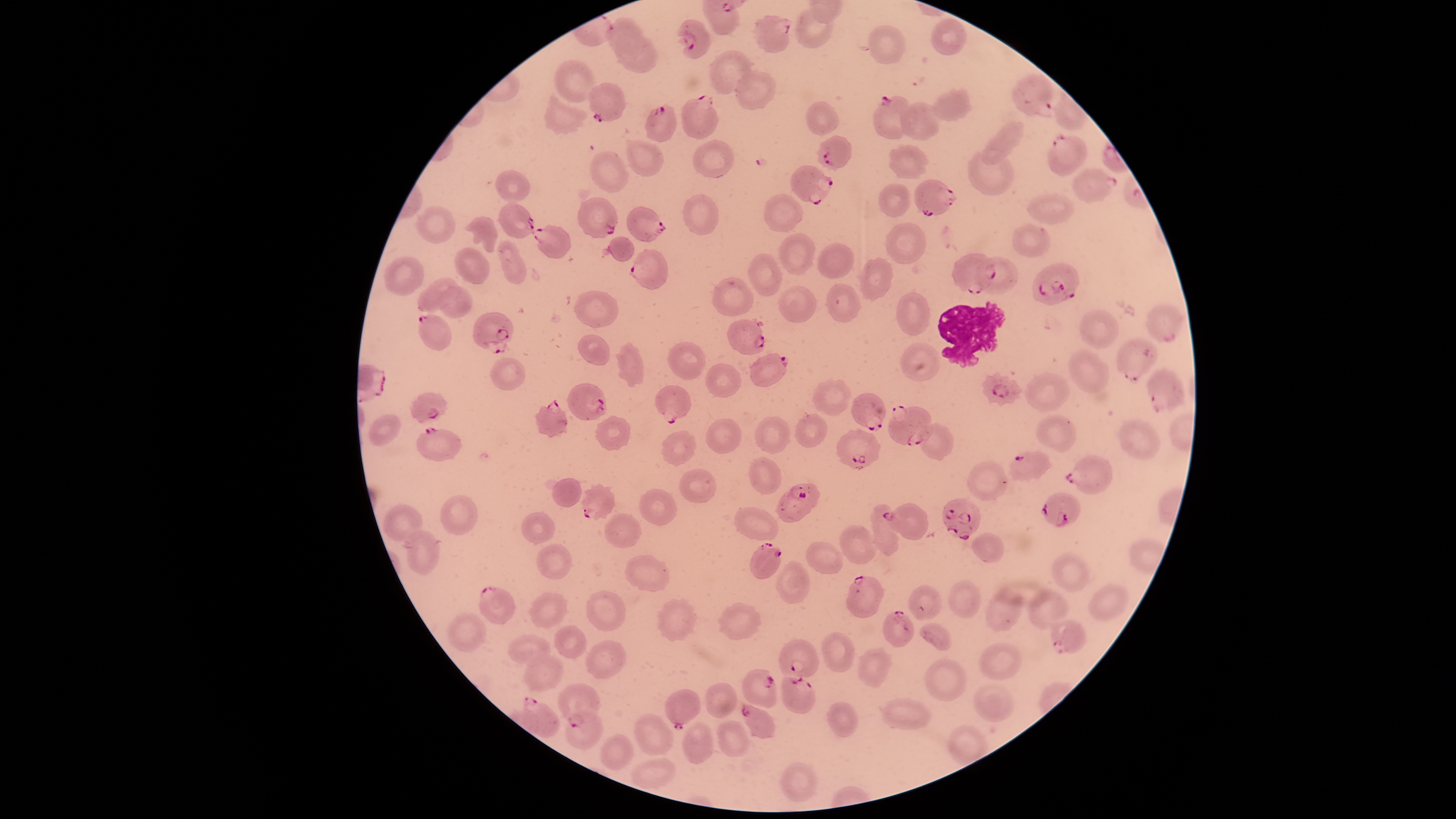

preparation = thin blood film
parasitized red blood cells = approximate bounding boxes as (left, top, right, bottom) in pixels: (753, 15, 792, 53), (677, 19, 710, 58), (1011, 74, 1053, 118), (590, 83, 626, 123), (680, 96, 718, 139), (872, 96, 917, 139), (644, 103, 677, 141), (1048, 132, 1086, 175), (816, 135, 852, 170), (791, 166, 834, 206), (1073, 168, 1118, 203), (915, 180, 955, 216), (579, 197, 617, 238), (498, 202, 534, 238), (626, 206, 666, 242), (532, 224, 570, 258), (629, 248, 666, 290), (952, 254, 995, 295), (1032, 262, 1079, 303), (826, 283, 862, 321), (1148, 303, 1183, 341), (471, 312, 513, 355), (418, 315, 450, 351), (727, 319, 765, 354), (1118, 338, 1158, 382), (748, 354, 789, 387), (1146, 368, 1185, 414), (981, 372, 1021, 407), (568, 383, 606, 420), (655, 385, 694, 424), (411, 392, 447, 422), (850, 392, 886, 431), (534, 400, 568, 437), (888, 405, 932, 445), (416, 427, 463, 460), (836, 429, 880, 470), (1009, 451, 1054, 482), (1065, 455, 1112, 495), (581, 483, 615, 520), (775, 483, 821, 522), (1041, 493, 1080, 526), (942, 498, 980, 540), (881, 502, 929, 539), (750, 541, 781, 579), (845, 575, 884, 619), (479, 586, 515, 624), (882, 610, 914, 647), (1050, 619, 1086, 654), (778, 639, 819, 678), (743, 669, 777, 707), (782, 675, 816, 714), (557, 685, 600, 727), (666, 689, 701, 731), (521, 698, 560, 737), (741, 705, 775, 738)
image size = 1456×819 pixels
uninfected red blood cells = approximate bounding boxes as (left, top, right, bottom) in pixels: (796, 6, 832, 47), (605, 17, 642, 53), (931, 19, 967, 57), (869, 25, 904, 64), (614, 32, 658, 72), (708, 50, 751, 95), (554, 60, 599, 102), (735, 71, 777, 110), (926, 87, 971, 122), (544, 92, 588, 136), (806, 101, 839, 135), (900, 103, 940, 141), (982, 123, 1023, 164), (626, 141, 665, 177), (692, 141, 735, 177), (888, 144, 929, 178), (590, 150, 629, 192), (967, 150, 1014, 194), (495, 170, 530, 202), (879, 184, 910, 218), (1027, 193, 1075, 225), (683, 194, 719, 234), (764, 194, 803, 233), (416, 205, 455, 245), (466, 216, 498, 252), (886, 223, 926, 264), (1013, 224, 1051, 255), (779, 233, 816, 275), (608, 235, 635, 261), (500, 240, 526, 284), (816, 243, 853, 277), (455, 247, 491, 285), (748, 254, 782, 297), (383, 256, 424, 297), (858, 256, 893, 301), (975, 257, 1018, 293), (712, 277, 754, 315), (417, 279, 459, 312), (778, 285, 817, 322), (439, 286, 473, 319), (575, 290, 619, 327), (895, 292, 929, 334), (1079, 309, 1119, 350), (577, 335, 608, 365), (616, 341, 644, 387), (668, 341, 707, 380), (900, 342, 942, 381), (1068, 349, 1110, 394), (490, 358, 524, 390), (705, 363, 741, 396), (1024, 372, 1070, 411), (811, 379, 851, 414), (794, 414, 827, 447), (1037, 414, 1077, 453), (369, 415, 400, 444), (595, 415, 631, 451), (755, 416, 789, 453), (705, 418, 742, 453), (1118, 420, 1160, 459), (921, 424, 953, 460), (661, 431, 696, 466), (749, 456, 780, 494), (968, 460, 1008, 500), (679, 469, 717, 504), (553, 478, 583, 508), (638, 487, 677, 526), (440, 495, 477, 535), (872, 504, 898, 557), (383, 505, 421, 541), (734, 506, 778, 539), (521, 513, 555, 544), (603, 513, 641, 548), (840, 524, 875, 566), (405, 531, 440, 575), (973, 531, 1004, 562), (536, 542, 572, 579), (805, 542, 845, 573), (1053, 553, 1090, 591), (626, 555, 669, 591), (776, 560, 810, 603), (949, 580, 981, 617), (1090, 583, 1128, 619), (986, 588, 1022, 631), (1028, 588, 1068, 630), (586, 591, 626, 631), (529, 592, 567, 628), (657, 598, 697, 641), (718, 603, 762, 641), (446, 613, 485, 652), (920, 624, 952, 650), (554, 625, 586, 659), (821, 632, 854, 672), (509, 635, 550, 665), (585, 641, 626, 678), (979, 644, 1022, 679), (858, 646, 892, 688), (524, 654, 562, 693), (925, 658, 966, 700), (706, 683, 736, 718), (975, 684, 1013, 721), (880, 699, 931, 729), (825, 702, 858, 737), (564, 709, 603, 750), (633, 712, 673, 756), (682, 721, 713, 763), (718, 721, 750, 756), (599, 734, 636, 770), (630, 759, 675, 788), (780, 763, 817, 802)
capture = smartphone photograph through the microscope eyepiece
species = Plasmodium falciparum
visible region = circular
stain = Giemsa
white blood cells = approximate bounding boxes as (left, top, right, bottom) in pixels: (937, 301, 1006, 369)
field of view = single
presence = malaria parasites identified